Describe the morphology of the erythrocytes.
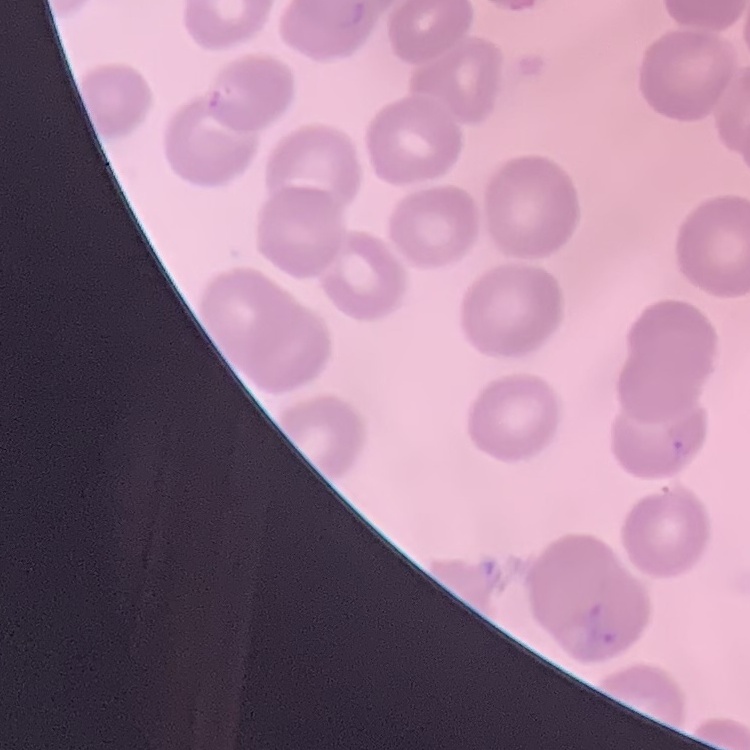

No rouleaux formation.

Summary:
  - Stain: Field's or Giemsa
  - Preparation: thin blood smear
  - Image type: one tile cut from a larger photomicrograph